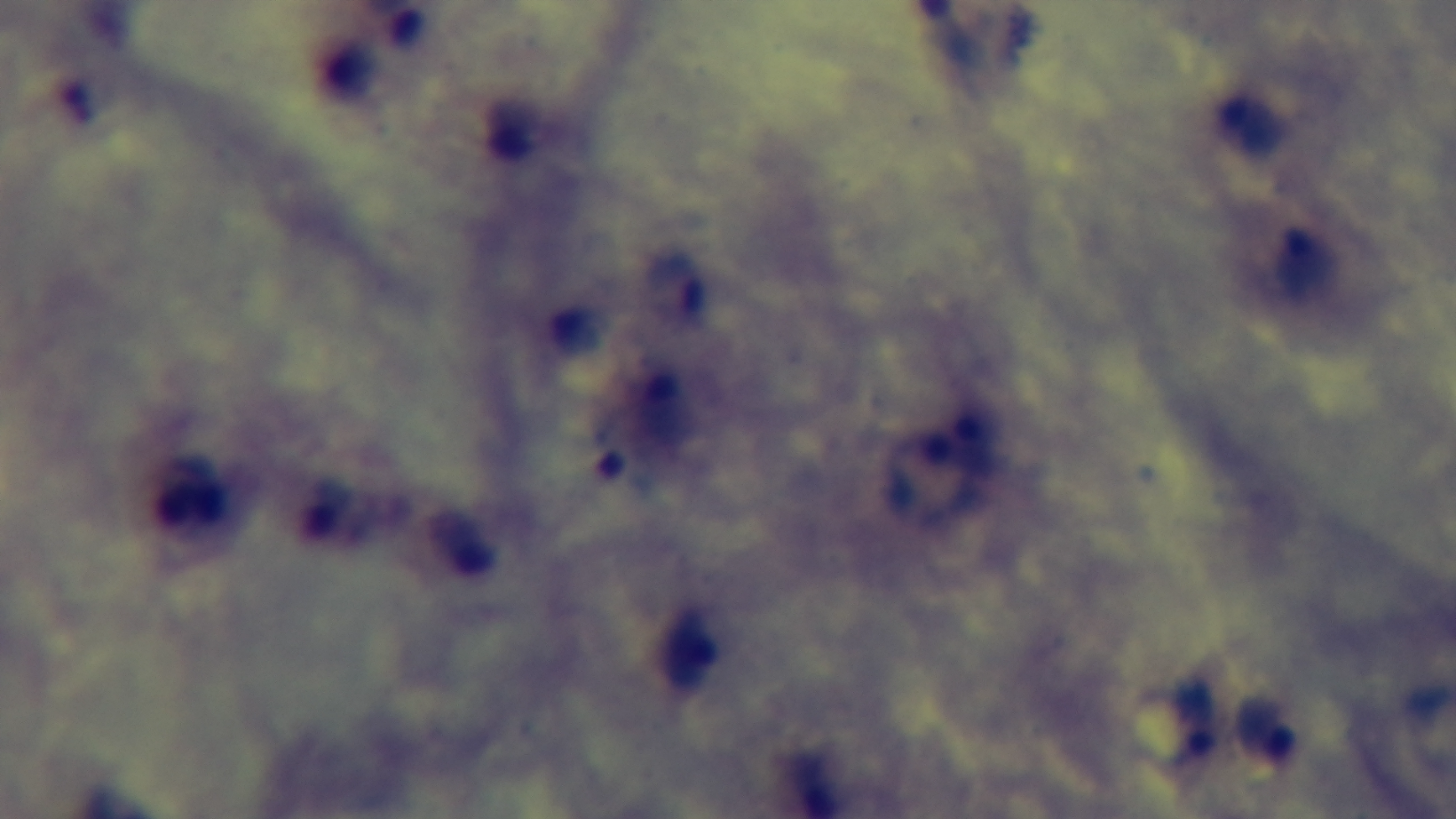 Light microscopy. One field from the slide. Malaria status: positive. Captured with a mounted 4K digital camera. Oil-immersion objective, 100x. Preparation: thick. Giemsa-stained.